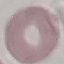
Summary:
  - Malaria status: uninfected
  - Capture: smartphone camera at the microscope eyepiece
  - Image type: automatically extracted cell patch, resized to 64 × 64 pixels
  - Stain: Giemsa
  - Preparation: thin smear